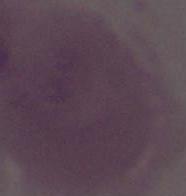

Photomicrograph. A red blood cell is seen. Captured at 1000x magnification.